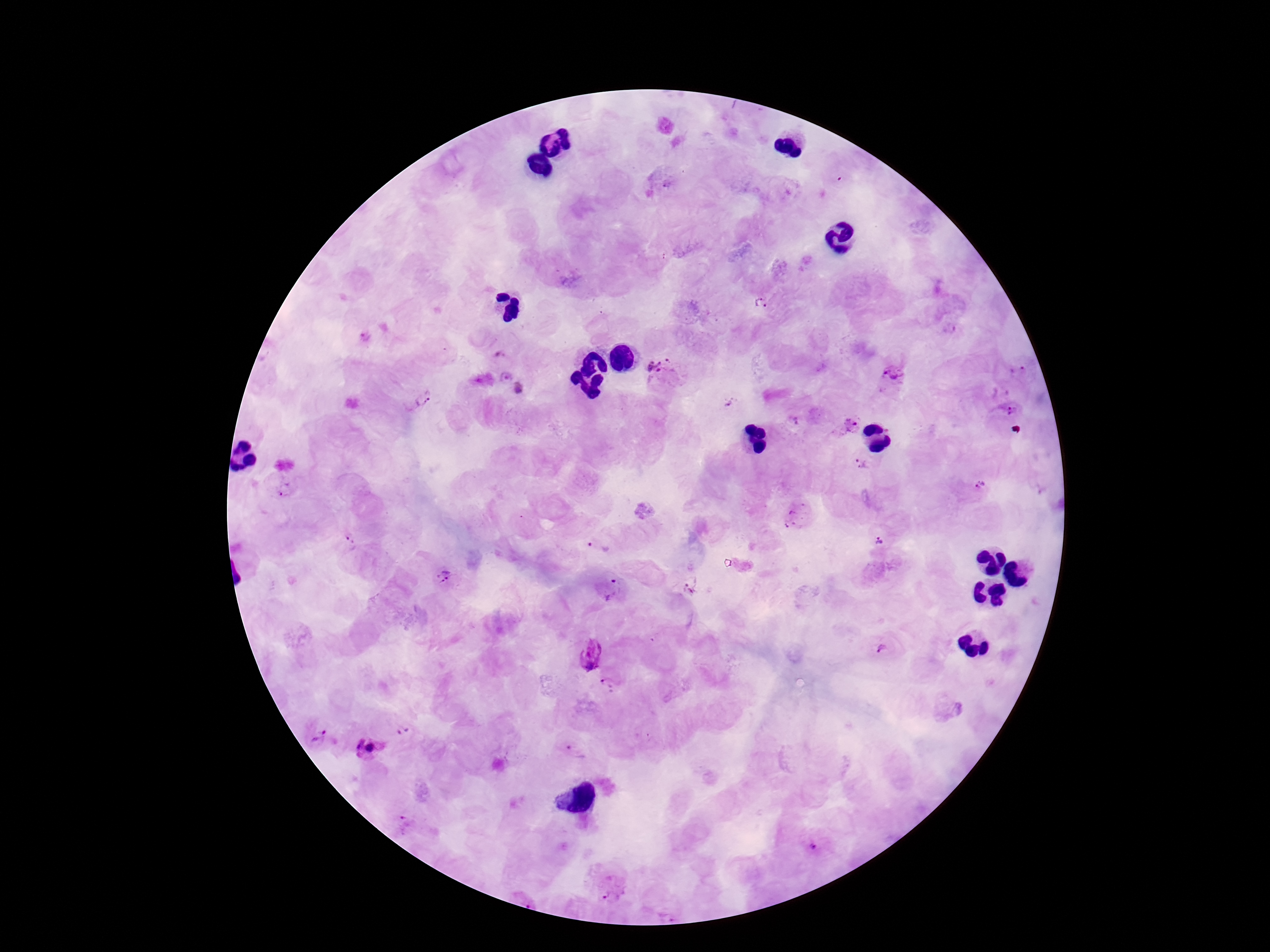

{
  "field_of_view": "one from this slide",
  "magnification": "100x",
  "plasmodium_parasite_locations": "approximate object centers, in pixels from the top-left corner: (x=761, y=303), (x=662, y=370), (x=1024, y=377), (x=893, y=378), (x=519, y=387), (x=422, y=398), (x=1009, y=409), (x=852, y=424), (x=863, y=464), (x=979, y=484), (x=285, y=488), (x=878, y=538), (x=349, y=541), (x=599, y=545), (x=444, y=577), (x=612, y=588), (x=883, y=650), (x=593, y=652), (x=609, y=684), (x=403, y=732), (x=320, y=736), (x=368, y=750), (x=577, y=752), (x=814, y=845), (x=614, y=889)",
  "patient_malaria_status": "infected",
  "preparation": "thick blood smear",
  "image_size": "1270×952 pixels",
  "stain": "Giemsa",
  "capture": "smartphone camera through the microscope eyepiece"
}